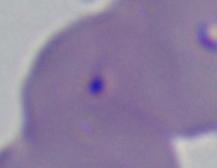
A Babesia parasite is seen. Captured at 1000x magnification. Photomicrograph.